Classify this cell by malaria status.
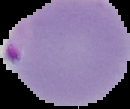

Parasitized.

Summary:
  - Image type: segmented cell region with the area outside set to black
  - Preparation: thin blood film
  - Image size: 130×109 pixels